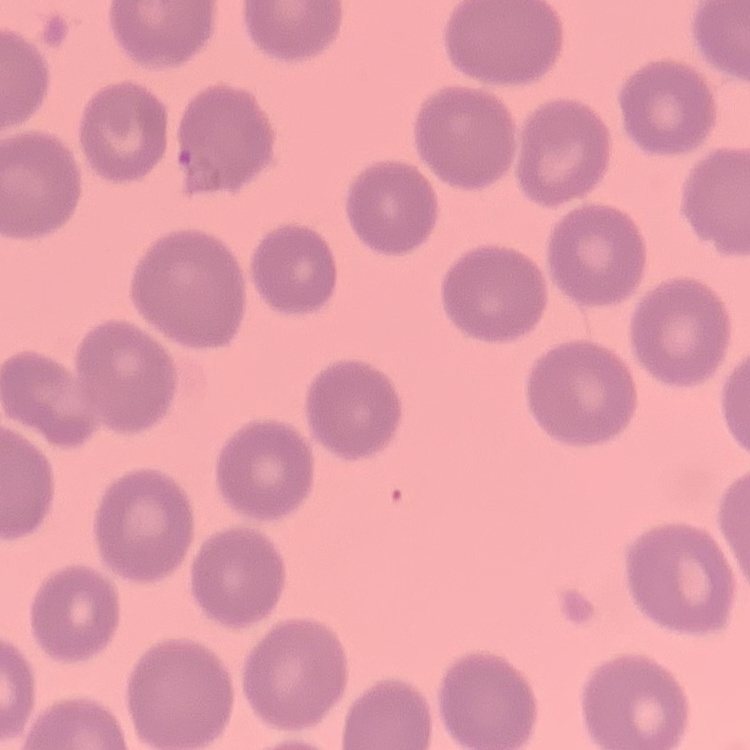

Summary:
  - Erythrocyte morphology: no rouleaux formation
  - Preparation: thin blood film
  - Stain: Field's or Giemsa
  - Image type: square crop of a larger photomicrograph